Give the position of every leukocyte visible.
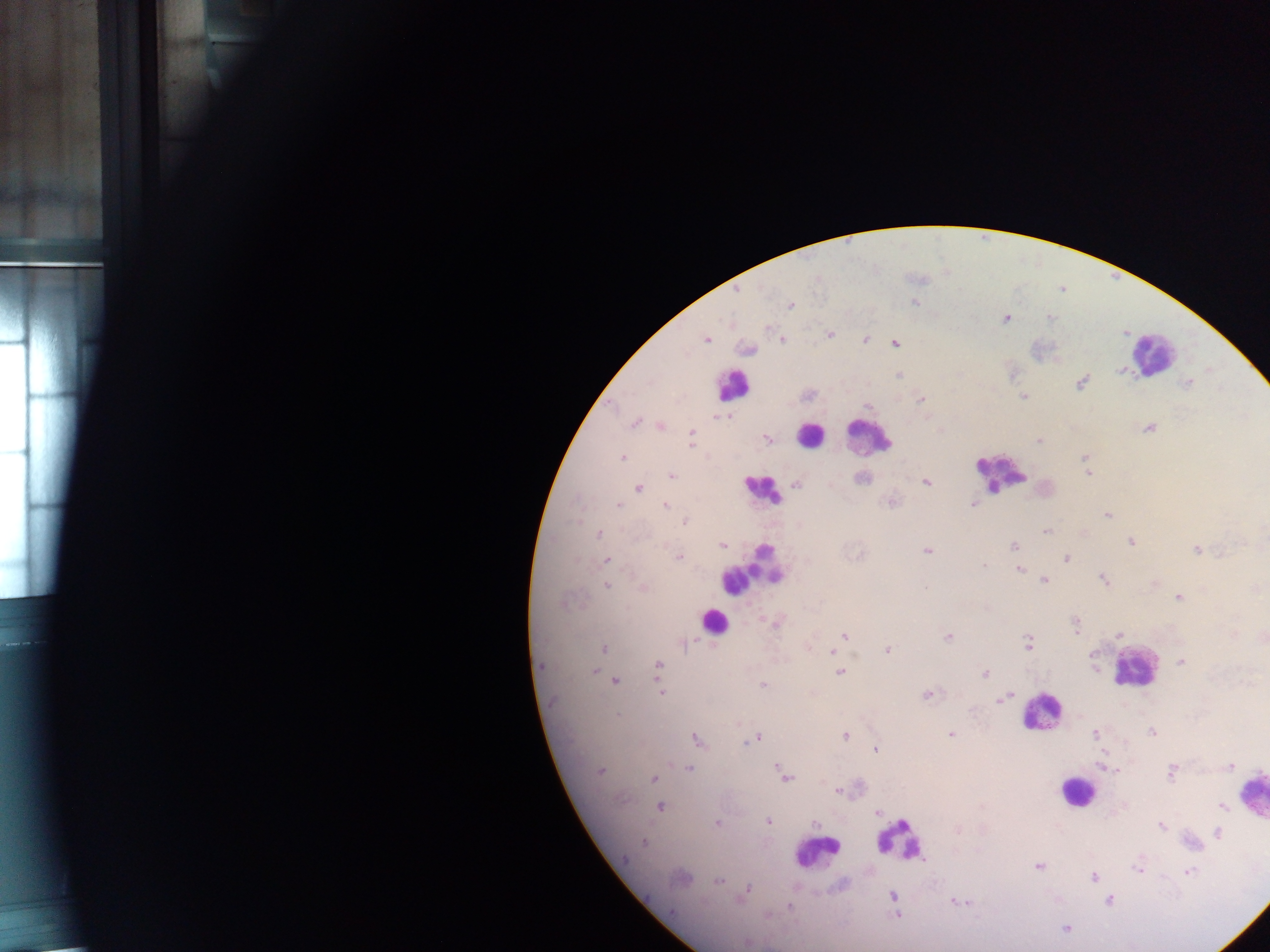

Approximate centers as x y in pixels.
Leukocytes: 1151 353; 733 385; 810 435; 868 435; 1000 473; 763 490; 752 571; 714 621; 1133 668; 1041 712; 1076 791; 1251 794; 900 839; 816 853.

capture = mobile-phone photograph through a microscope
image size = 1270×952 pixels
field of view = single
preparation = thick blood smear
Plasmodium parasite locations = approximate centers as x y in pixels: 736 292; 915 302; 791 305; 1005 319; 829 334; 706 339; 782 339; 865 339; 895 343; 1120 370; 899 375; 1081 382; 1188 382; 1023 397; 922 399; 867 406; 727 416; 717 417; 634 423; 662 427; 1148 429; 692 434; 767 438; 691 441; 1039 442; 622 458; 1085 459; 1088 472; 671 475; 862 479; 926 482; 796 484; 638 488; 977 500; 890 502; 618 506; 665 507; 1107 516; 685 522; 1046 532; 599 533; 1131 541; 722 545; 1013 546; 1197 549; 927 551; 860 555; 679 556; 1066 558; 607 560; 983 565; 1019 569; 1044 580; 1103 580; 606 585; 643 587; 1256 589; 1178 597; 564 602; 775 624; 1076 624; 1119 635; 843 636; 948 637; 1028 643; 683 645; 837 646; 603 649; 888 651; 831 652; 1181 662; 658 665; 542 666; 595 672; 840 673; 985 674; 615 681; 763 685; 661 691; 927 695; 1002 699; 618 715; 1151 732; 1095 734; 846 735; 951 735; 756 738; 698 740; 748 741; 875 749; 691 764; 1103 766; 1229 766; 688 768; 601 770; 782 772; 1171 772; 785 777; 653 778; 838 791; 660 806; 1222 806; 877 812; 768 821; 717 824; 815 824; 1160 825; 1218 833; 644 842; 1038 866; 1138 869; 1188 872; 1093 877; 717 881; 746 893; 892 896; 1109 901; 960 903; 790 906; 767 915; 896 915; 1065 928; 747 942
country = Ghana